Name the blood parasite species.
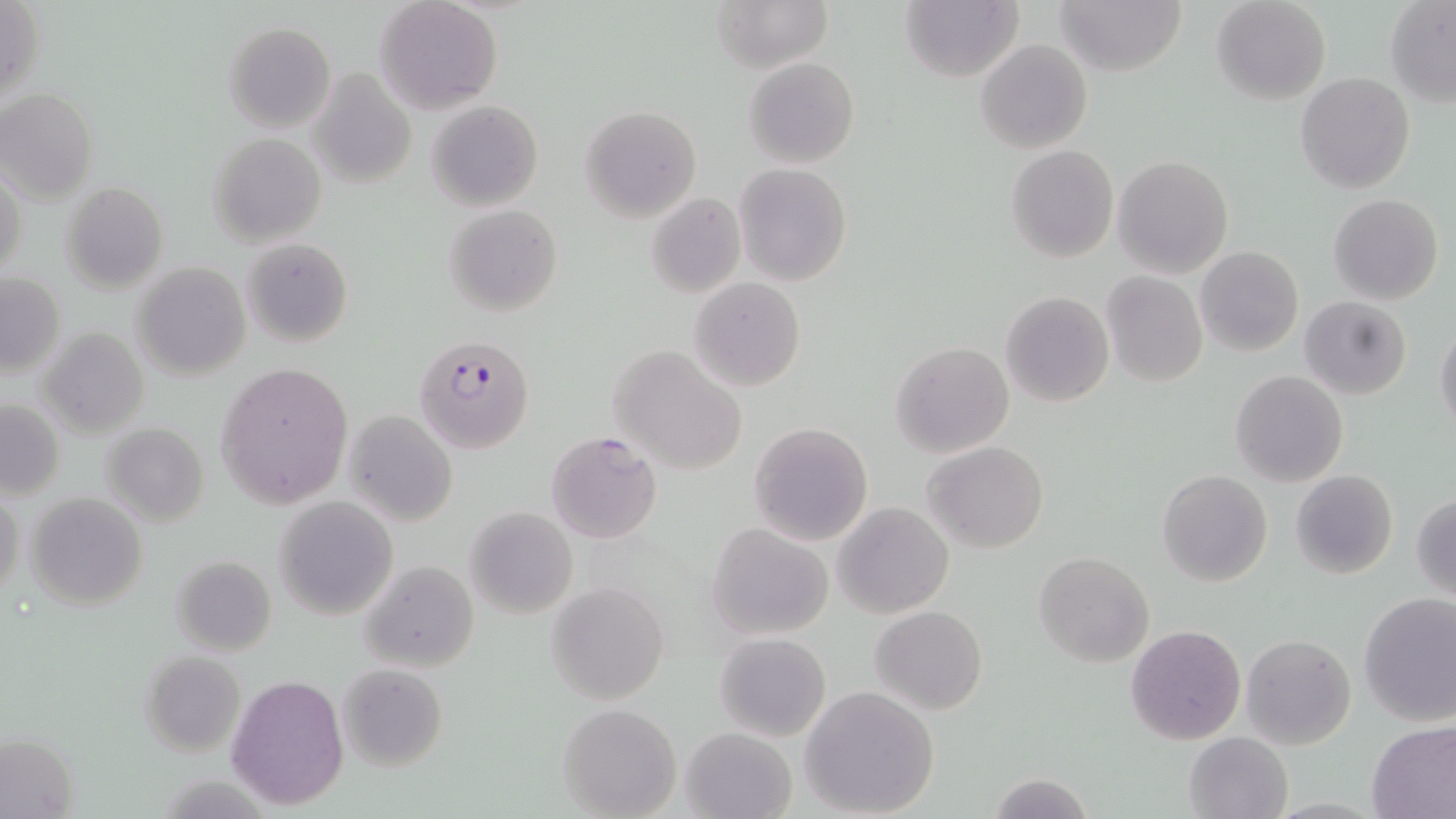
Plasmodium falciparum.

Approximate bounding boxes as [x1, y1, x2, y2] in pixels. Plasmodium falciparum-infected red blood cell locations: [417, 333, 537, 456]. Uninfected red blood cell locations: [376, 0, 502, 114], [713, 0, 831, 72], [1053, 0, 1187, 76], [1212, 0, 1330, 105], [0, 1, 46, 107], [900, 1, 1022, 82], [1384, 2, 1455, 106], [224, 22, 335, 132], [974, 39, 1092, 154], [743, 57, 860, 169], [309, 67, 416, 189], [1296, 73, 1415, 193], [0, 87, 98, 202], [427, 100, 542, 211], [579, 104, 702, 223], [208, 133, 326, 246], [1006, 145, 1118, 262], [1112, 155, 1233, 277], [1, 163, 27, 282], [735, 163, 853, 286], [60, 181, 169, 292], [645, 192, 745, 299], [1330, 193, 1443, 305], [445, 204, 562, 317], [243, 237, 353, 348], [1194, 247, 1304, 358], [131, 261, 252, 381], [0, 271, 65, 379], [1101, 271, 1208, 387], [689, 278, 806, 392], [1000, 291, 1114, 409], [1300, 296, 1412, 399], [1435, 323, 1456, 436], [39, 327, 149, 440], [891, 340, 1014, 457], [608, 344, 749, 476], [214, 362, 354, 510], [1231, 370, 1348, 487], [0, 400, 64, 500], [344, 409, 459, 528], [102, 421, 209, 526], [748, 421, 873, 545], [544, 430, 662, 544], [922, 440, 1050, 553], [1157, 469, 1272, 587], [1289, 469, 1398, 579], [0, 488, 24, 601], [1412, 491, 1456, 599], [25, 492, 147, 608], [273, 495, 398, 620], [834, 502, 953, 618], [466, 507, 577, 619], [706, 522, 834, 640], [1033, 551, 1155, 667], [170, 556, 276, 658], [359, 559, 478, 674], [546, 582, 669, 703], [1358, 592, 1456, 726], [870, 605, 987, 715], [1125, 624, 1246, 746], [715, 633, 832, 741], [1241, 634, 1356, 748], [140, 651, 247, 757], [337, 663, 447, 771], [226, 673, 349, 809], [799, 686, 940, 817], [558, 702, 681, 818], [1366, 720, 1456, 819], [680, 727, 798, 819], [1183, 731, 1294, 819], [0, 733, 80, 818], [989, 773, 1092, 819]. Image is 1456×819 pixels. Thin blood film. One field of a larger specimen. Light microscopy. 1000x magnification. May-Grünwald-Giemsa stain.